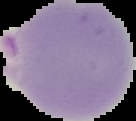

Image is 136×121 pixels. Malaria status: parasitized. Segmented cell region on a black background. From a thin blood film.